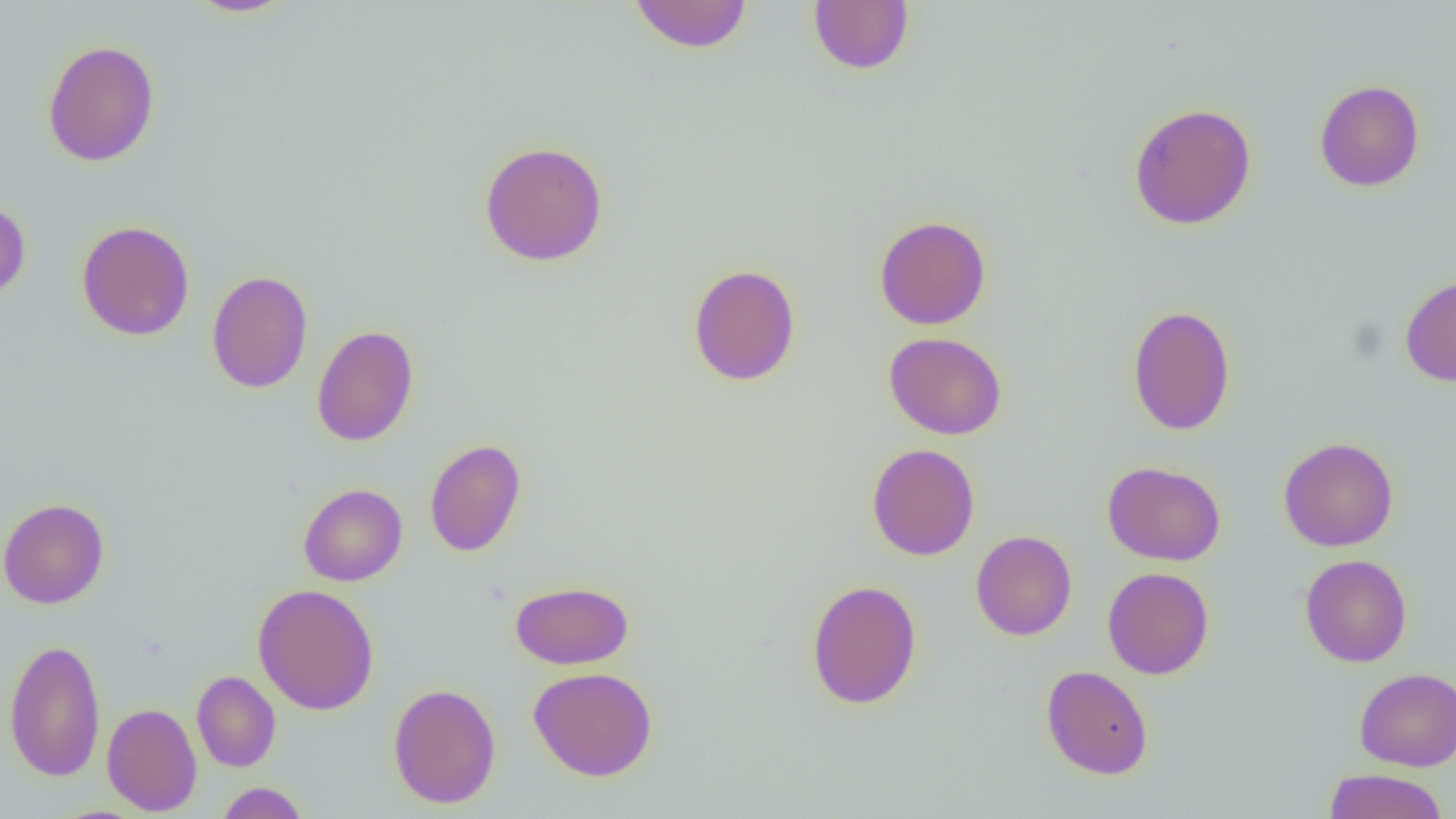

slide-level diagnosis = negative for blood parasites
image size = 1456×819 pixels
magnification = 1000x
field of view = single
modality = optical microscopy
uninfected red blood cell locations = approximate bounding boxes as (x1, y1, x2, y2) in pixels: (183, 0, 297, 18), (628, 1, 752, 53), (808, 1, 914, 75), (42, 39, 160, 167), (1314, 80, 1424, 192), (1128, 102, 1257, 230), (479, 140, 608, 267), (0, 196, 31, 303), (873, 214, 992, 330), (76, 220, 195, 341), (687, 263, 801, 386), (206, 269, 313, 394), (1399, 274, 1456, 387), (1127, 304, 1236, 436), (311, 324, 419, 447), (884, 332, 1007, 440), (1278, 436, 1398, 552), (424, 438, 526, 557), (866, 443, 980, 561), (1102, 461, 1226, 566), (298, 483, 408, 586), (0, 497, 110, 609), (971, 530, 1077, 641), (1299, 554, 1412, 667), (1102, 567, 1214, 679), (806, 579, 922, 710), (510, 580, 634, 669), (253, 583, 380, 715), (4, 637, 106, 782), (1040, 665, 1153, 779), (528, 666, 658, 781), (1354, 667, 1456, 771), (192, 670, 281, 772), (388, 682, 502, 809), (102, 702, 202, 815), (1323, 768, 1449, 819), (216, 782, 310, 819)
preparation = thin blood smear